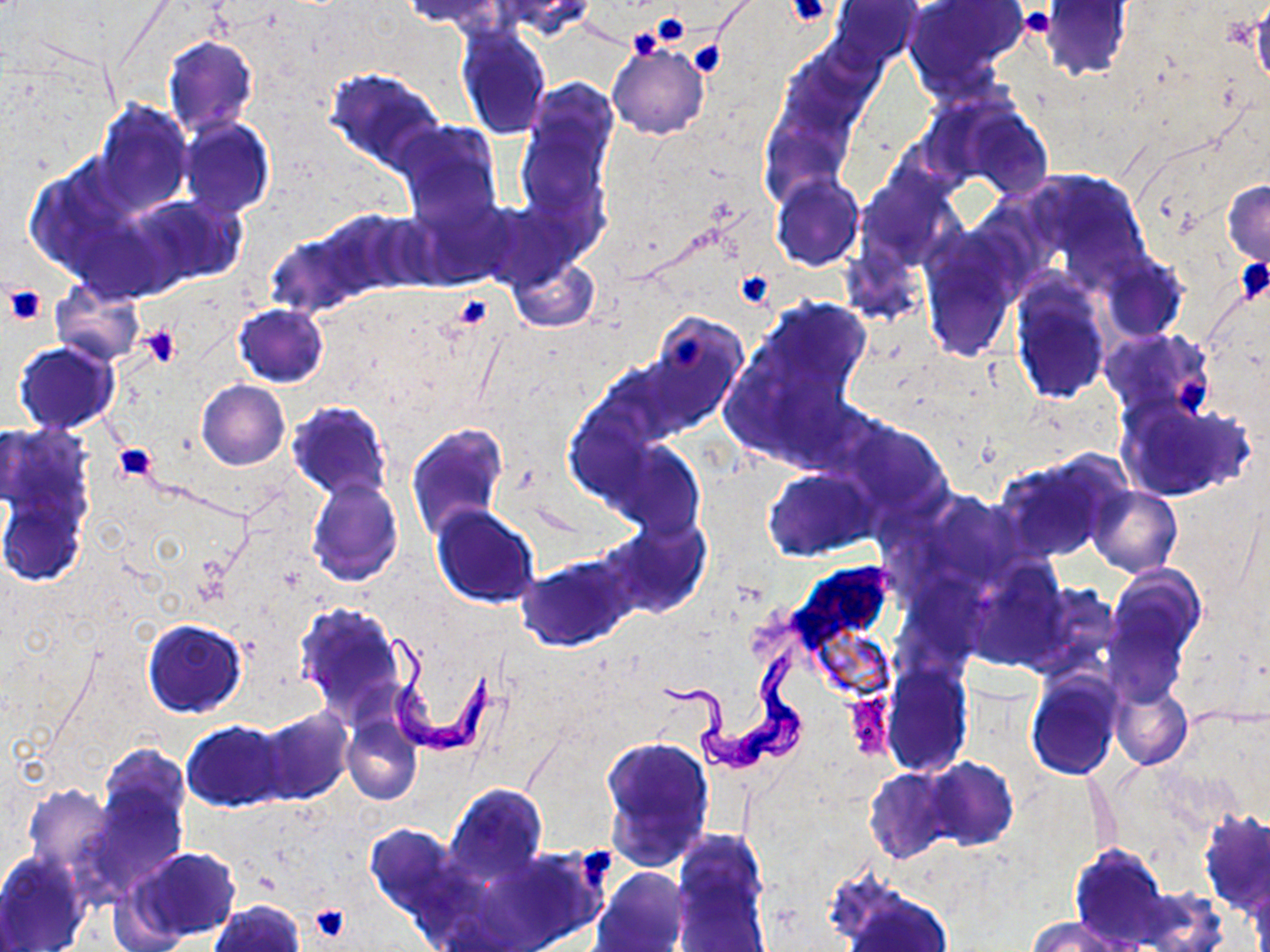
slide-level diagnosis = Trypanosoma brucei
uninfected red blood cell locations = approximate bounding boxes as (x1,y1)-(x2,y2) corner pairs in pixels: (401,0)-(504,31), (492,0)-(598,39), (831,0)-(922,67), (1042,2)-(1132,80), (906,3)-(1019,91), (454,26)-(553,140), (163,35)-(258,138), (608,43)-(709,139), (324,67)-(445,174), (518,93)-(613,231), (92,99)-(193,216), (961,105)-(1054,199), (179,117)-(274,221), (393,121)-(502,231), (1035,171)-(1140,264), (861,174)-(948,264), (772,175)-(863,272), (1222,182)-(1270,267), (127,192)-(245,290), (405,194)-(517,291), (301,207)-(429,304), (267,221)-(379,317), (920,240)-(1018,359), (508,256)-(598,332), (1102,257)-(1186,342), (1011,279)-(1111,406), (50,281)-(145,365), (762,300)-(871,398), (234,304)-(328,387), (637,314)-(747,438), (1101,328)-(1212,419), (14,341)-(120,434), (196,380)-(289,470), (1116,394)-(1256,503), (287,400)-(393,501), (839,416)-(950,518), (406,422)-(508,541), (611,443)-(704,540), (993,455)-(1122,563), (764,467)-(879,561), (1,470)-(90,590), (306,478)-(402,586), (1088,485)-(1182,578), (919,492)-(1027,593), (431,505)-(540,609), (601,519)-(710,618), (518,556)-(634,650), (1107,566)-(1205,667), (1104,597)-(1190,703), (293,603)-(410,722), (142,618)-(248,717), (883,663)-(972,774), (1027,669)-(1123,780), (1110,682)-(1192,770), (254,708)-(353,805), (342,715)-(422,804), (183,720)-(288,811), (599,735)-(715,869), (97,744)-(190,839), (923,757)-(1019,851), (864,767)-(958,863), (1087,772)-(1119,859), (85,775)-(186,890), (21,782)-(118,878), (444,782)-(547,887), (1198,811)-(1270,916), (364,823)-(464,924), (1069,845)-(1170,948), (127,847)-(241,942), (671,847)-(772,950), (0,852)-(88,951), (594,868)-(690,952), (835,882)-(955,952), (208,901)-(304,952), (1030,917)-(1124,952)
image size = 1270×952 pixels
Trypanosoma brucei locations = approximate bounding boxes as (x1,y1)-(x2,y2) corner pairs in pixels: (378,630)-(501,756), (661,648)-(811,774)
platelet locations = approximate bounding boxes as (x1,y1)-(x2,y2) corner pairs in pixels: (787,0)-(833,27), (1020,7)-(1056,39), (651,12)-(690,47), (637,17)-(685,59), (626,27)-(665,62), (688,40)-(725,78), (1236,257)-(1269,306), (733,272)-(775,308), (4,286)-(46,325), (450,293)-(491,328), (141,325)-(182,368), (667,331)-(708,370), (1175,375)-(1216,419), (112,444)-(158,482), (578,845)-(616,887), (308,903)-(351,942)
field of view = one of a larger specimen
stain = May-Grünwald-Giemsa
modality = optical microscopy
preparation = thin blood film
magnification = 1000x